Name the parasite shown.
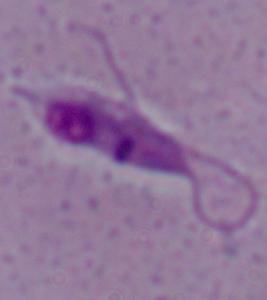

Leishmania.

Photomicrograph. Captured at 1000x magnification.